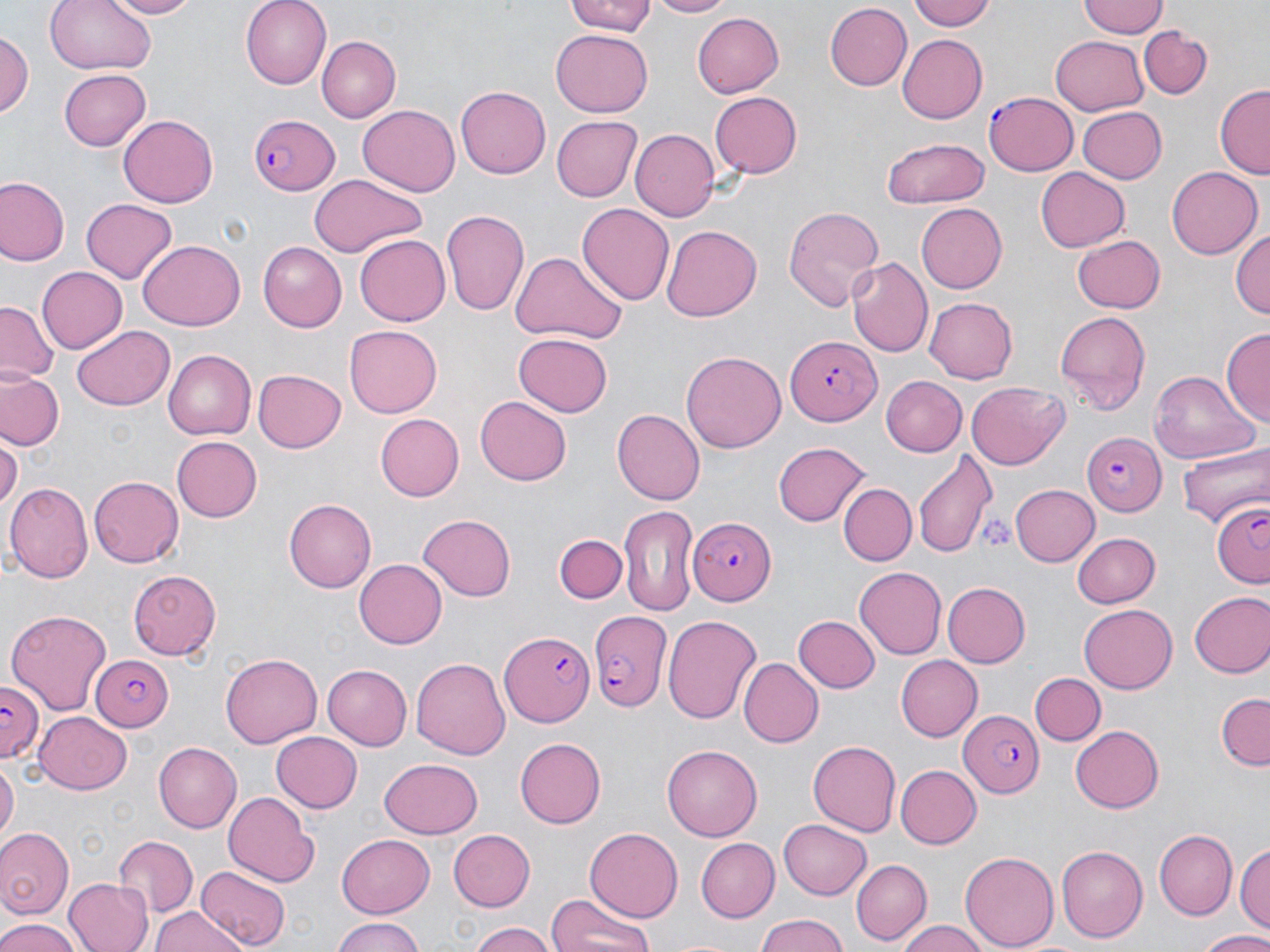

slide_level_diagnosis: Plasmodium falciparum
image_size: 1270×952 pixels
preparation: thin blood smear
uninfected_red_blood_cell_locations: 'approximate bounding boxes as named x1/y1/x2/y2 corners in pixels: (x1=44, y1=0, x2=158, y2=77), (x1=100, y1=0, x2=201, y2=18), (x1=242, y1=0, x2=334, y2=88), (x1=565, y1=0, x2=660, y2=37), (x1=642, y1=0, x2=738, y2=18), (x1=909, y1=0, x2=998, y2=32), (x1=1077, y1=0, x2=1169, y2=40), (x1=824, y1=3, x2=911, y2=90), (x1=691, y1=11, x2=783, y2=97), (x1=1139, y1=26, x2=1214, y2=99), (x1=2, y1=28, x2=32, y2=123), (x1=550, y1=30, x2=653, y2=115), (x1=897, y1=32, x2=987, y2=121), (x1=1050, y1=35, x2=1149, y2=115), (x1=316, y1=36, x2=399, y2=121), (x1=59, y1=67, x2=149, y2=148), (x1=1215, y1=84, x2=1269, y2=180), (x1=454, y1=88, x2=549, y2=180), (x1=709, y1=91, x2=802, y2=178), (x1=357, y1=103, x2=460, y2=195), (x1=1077, y1=106, x2=1167, y2=184), (x1=119, y1=113, x2=218, y2=207), (x1=550, y1=113, x2=640, y2=199), (x1=628, y1=127, x2=719, y2=221), (x1=881, y1=138, x2=990, y2=208), (x1=1036, y1=167, x2=1130, y2=252), (x1=1167, y1=167, x2=1261, y2=259), (x1=308, y1=174, x2=426, y2=258), (x1=0, y1=177, x2=69, y2=265), (x1=79, y1=199, x2=178, y2=283), (x1=577, y1=201, x2=673, y2=302), (x1=914, y1=202, x2=1006, y2=293), (x1=783, y1=205, x2=885, y2=311), (x1=440, y1=207, x2=531, y2=320), (x1=661, y1=225, x2=763, y2=322), (x1=1230, y1=226, x2=1270, y2=318), (x1=355, y1=234, x2=450, y2=326), (x1=1073, y1=235, x2=1166, y2=312), (x1=138, y1=239, x2=245, y2=330), (x1=259, y1=242, x2=347, y2=332), (x1=510, y1=250, x2=627, y2=344), (x1=847, y1=257, x2=932, y2=357), (x1=36, y1=265, x2=126, y2=355), (x1=924, y1=297, x2=1018, y2=382), (x1=0, y1=303, x2=56, y2=382), (x1=1054, y1=309, x2=1151, y2=412), (x1=71, y1=325, x2=175, y2=410), (x1=345, y1=326, x2=442, y2=418), (x1=1222, y1=330, x2=1269, y2=427), (x1=514, y1=332, x2=612, y2=416), (x1=164, y1=350, x2=256, y2=439), (x1=679, y1=350, x2=786, y2=453), (x1=254, y1=368, x2=347, y2=453), (x1=1, y1=370, x2=66, y2=452), (x1=1151, y1=371, x2=1257, y2=462), (x1=882, y1=377, x2=967, y2=456), (x1=965, y1=381, x2=1070, y2=468), (x1=475, y1=396, x2=573, y2=486), (x1=612, y1=408, x2=705, y2=507), (x1=375, y1=412, x2=463, y2=500), (x1=1, y1=437, x2=21, y2=514), (x1=173, y1=437, x2=263, y2=522), (x1=1179, y1=438, x2=1269, y2=527), (x1=774, y1=441, x2=870, y2=527), (x1=911, y1=450, x2=997, y2=559), (x1=89, y1=474, x2=183, y2=566), (x1=6, y1=482, x2=91, y2=585), (x1=839, y1=483, x2=916, y2=565), (x1=1010, y1=483, x2=1100, y2=566), (x1=283, y1=499, x2=375, y2=592), (x1=618, y1=503, x2=701, y2=616), (x1=416, y1=515, x2=517, y2=602), (x1=1072, y1=531, x2=1162, y2=608), (x1=556, y1=532, x2=628, y2=605), (x1=355, y1=559, x2=448, y2=648), (x1=853, y1=565, x2=945, y2=660), (x1=127, y1=569, x2=222, y2=658), (x1=943, y1=581, x2=1030, y2=667), (x1=1188, y1=590, x2=1270, y2=678), (x1=1079, y1=605, x2=1177, y2=692), (x1=6, y1=610, x2=114, y2=717), (x1=663, y1=613, x2=761, y2=724), (x1=793, y1=615, x2=878, y2=693), (x1=220, y1=652, x2=322, y2=747), (x1=411, y1=655, x2=510, y2=760), (x1=896, y1=656, x2=983, y2=741), (x1=740, y1=659, x2=823, y2=745), (x1=325, y1=663, x2=412, y2=749), (x1=1031, y1=672, x2=1104, y2=746), (x1=1216, y1=692, x2=1269, y2=769), (x1=37, y1=709, x2=133, y2=792), (x1=1072, y1=727, x2=1165, y2=812), (x1=269, y1=731, x2=362, y2=813), (x1=515, y1=737, x2=607, y2=828), (x1=806, y1=740, x2=900, y2=837), (x1=153, y1=742, x2=241, y2=832), (x1=662, y1=745, x2=763, y2=840), (x1=380, y1=757, x2=482, y2=838), (x1=1, y1=761, x2=17, y2=845), (x1=896, y1=765, x2=982, y2=848), (x1=223, y1=792, x2=318, y2=886), (x1=779, y1=817, x2=872, y2=900), (x1=0, y1=826, x2=73, y2=921), (x1=447, y1=829, x2=535, y2=912), (x1=586, y1=829, x2=683, y2=919), (x1=1155, y1=830, x2=1236, y2=918), (x1=114, y1=834, x2=200, y2=919), (x1=335, y1=834, x2=436, y2=917), (x1=1235, y1=836, x2=1270, y2=934), (x1=694, y1=837, x2=779, y2=921), (x1=1057, y1=845, x2=1149, y2=941), (x1=960, y1=851, x2=1057, y2=951), (x1=851, y1=858, x2=931, y2=944), (x1=196, y1=866, x2=290, y2=949), (x1=63, y1=877, x2=152, y2=952), (x1=548, y1=893, x2=657, y2=952), (x1=149, y1=908, x2=248, y2=952), (x1=751, y1=914, x2=853, y2=952), (x1=330, y1=917, x2=424, y2=952), (x1=0, y1=919, x2=82, y2=952), (x1=466, y1=922, x2=559, y2=952), (x1=896, y1=922, x2=994, y2=952), (x1=1193, y1=930, x2=1270, y2=951)'
stain: May-Grünwald-Giemsa
platelet_locations: 'approximate bounding boxes as named x1/y1/x2/y2 corners in pixels: (x1=982, y1=516, x2=1016, y2=554)'
plasmodium_falciparum_infected_red_blood_cell_locations: 'approximate bounding boxes as named x1/y1/x2/y2 corners in pixels: (x1=985, y1=89, x2=1081, y2=176), (x1=249, y1=110, x2=343, y2=197), (x1=784, y1=334, x2=880, y2=425), (x1=1080, y1=432, x2=1164, y2=515), (x1=1211, y1=500, x2=1270, y2=588), (x1=689, y1=517, x2=774, y2=605), (x1=587, y1=610, x2=671, y2=714), (x1=499, y1=630, x2=595, y2=727), (x1=89, y1=654, x2=176, y2=732), (x1=0, y1=681, x2=46, y2=764), (x1=957, y1=709, x2=1042, y2=797)'
magnification: 1000x
field_of_view: one of a larger specimen
modality: light microscopy